Report the malaria status of this cell.
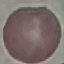

Uninfected.

Thin blood film. Automatically extracted cell patch, resized to 64 × 64 pixels. Giemsa-stained preparation. Acquired by smartphone through the microscope eyepiece.